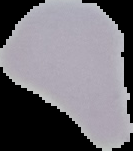

image_size: 133×151 pixels
image_type: cell region segmented out of the field of view; surrounding area masked to black
preparation: thin blood film
malaria_status: uninfected